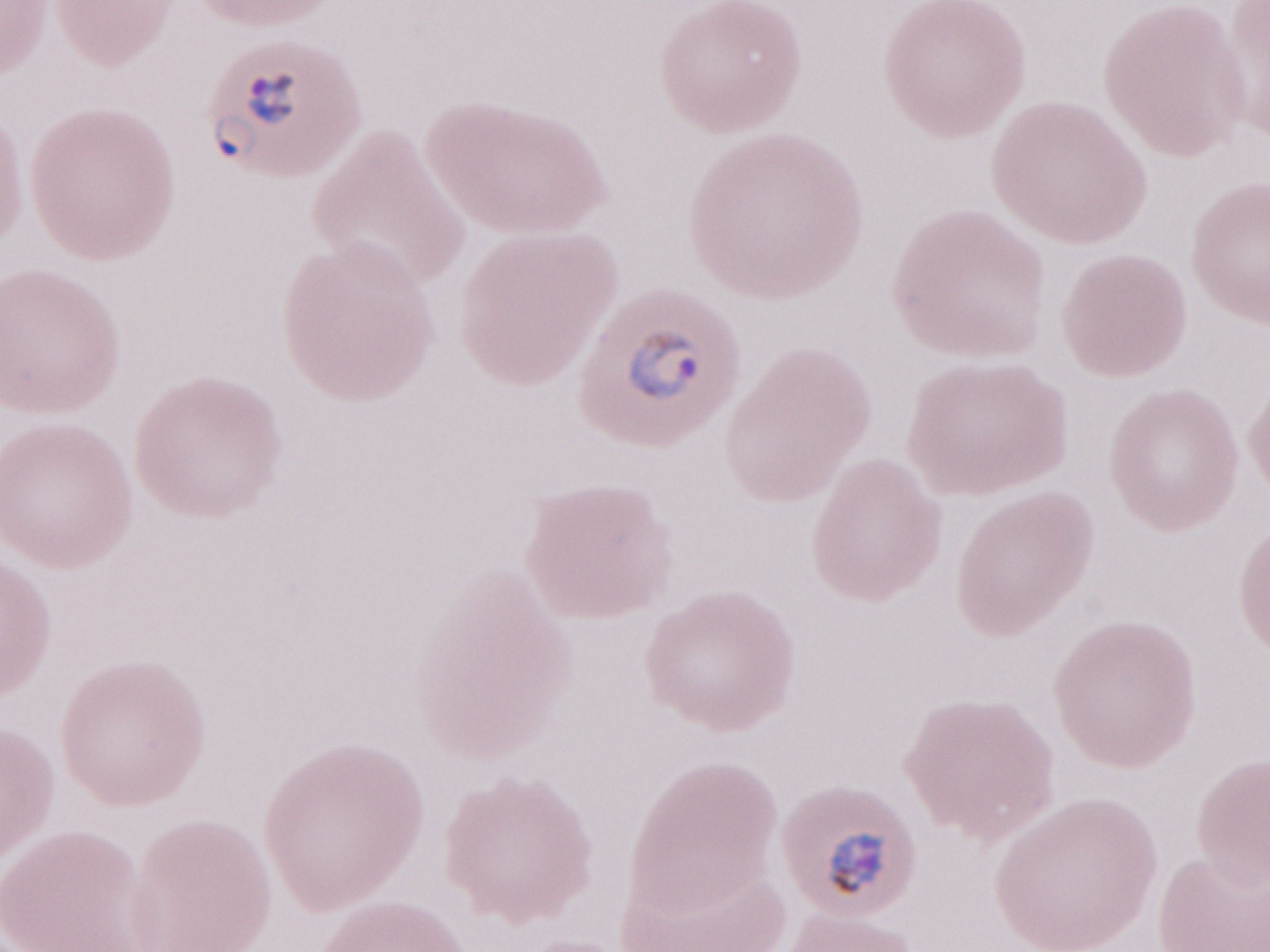

Single field of view. May-Grünwald-Giemsa stain. Patient-level malaria diagnosis: positive. 1,000x magnification. Olympus BX43 microscope and DP73 digital camera. Thin blood smear. Image is 1270×952 pixels.